Describe the morphology of the erythrocytes.
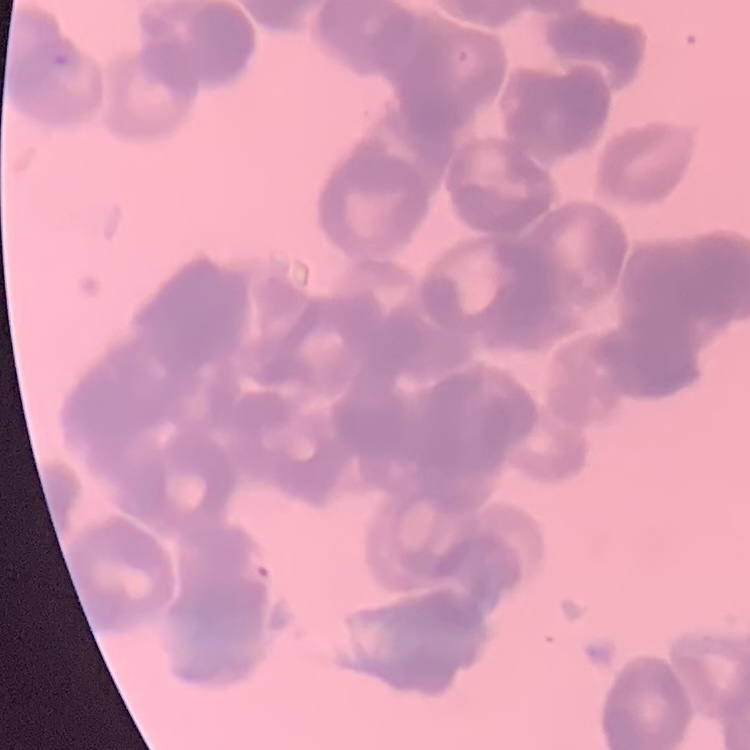

Rouleaux formation.

Summary:
  - Stain: Field's or Giemsa
  - Preparation: thin peripheral smear
  - Image type: square crop of a larger photomicrograph